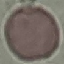

Summary:
  - Result: no malaria parasites detected
  - Stain: Giemsa
  - Capture: smartphone through the microscope eyepiece
  - Preparation: thin blood film
  - Image type: cell patch, automatically extracted from a larger field of view and resized to 64 × 64 pixels